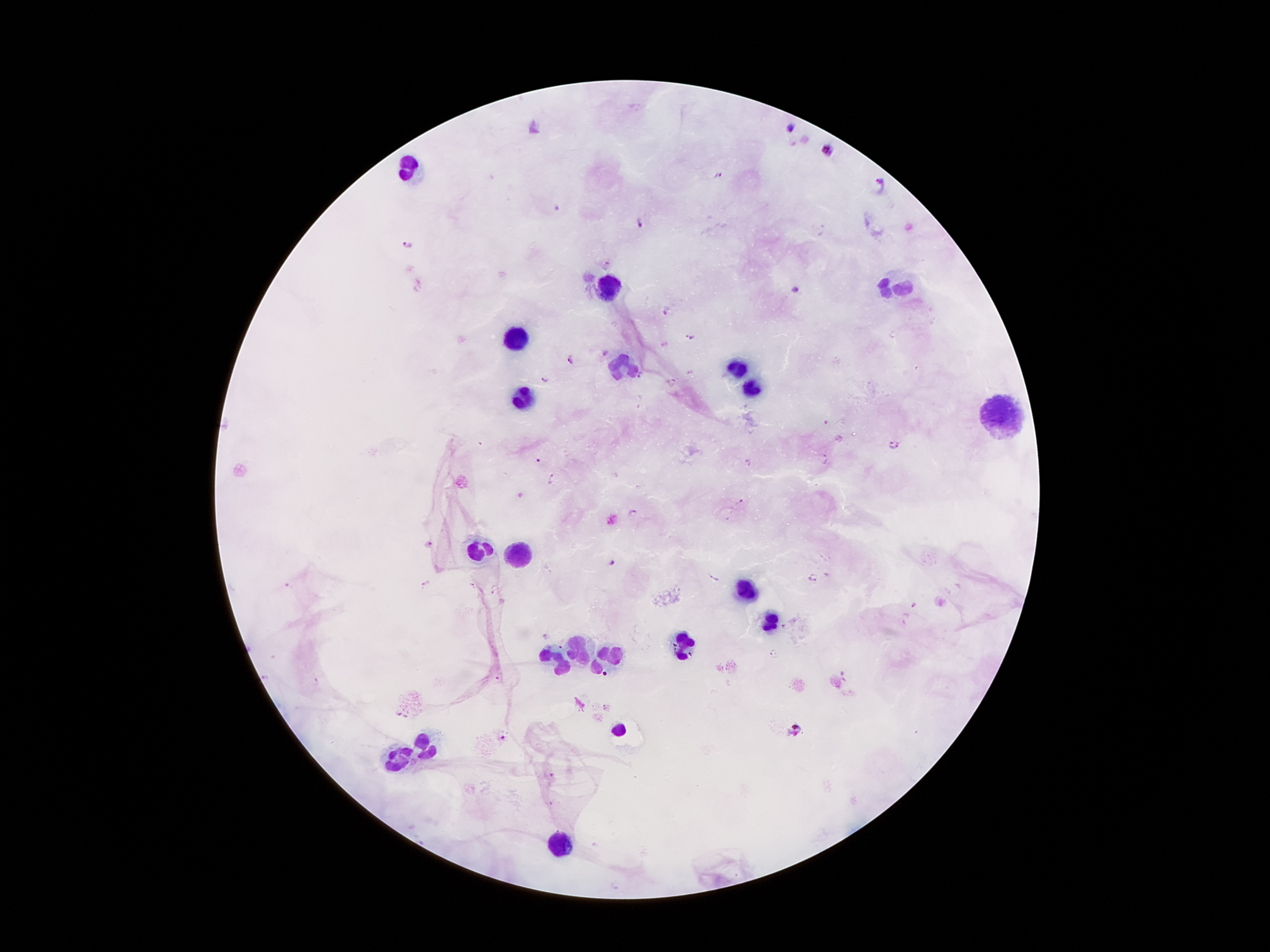

{
  "field_of_view": "one from this slide",
  "leukocyte_locations": "approximate centers as (x, y) in pixels: (408, 168), (609, 284), (897, 286), (517, 336), (622, 367), (739, 370), (752, 388), (523, 397), (1002, 412), (478, 552), (514, 554), (746, 588), (771, 620), (681, 641), (578, 648), (556, 659), (605, 659), (616, 731), (430, 745), (400, 755), (559, 843)",
  "stain": "Giemsa",
  "magnification": "100x",
  "image_size": "1270×952 pixels",
  "plasmodium_parasite_locations": "approximate centers as (x, y) in pixels: (789, 129), (828, 149), (717, 173), (880, 182), (555, 210), (639, 223), (407, 244), (796, 288), (667, 310), (689, 337), (605, 354), (570, 359), (641, 374), (547, 380), (673, 382), (827, 422), (893, 444), (824, 458), (538, 461), (749, 463), (551, 478), (739, 501), (631, 513), (429, 545), (613, 564), (814, 577), (713, 578), (427, 583), (289, 584), (473, 586), (495, 589), (915, 605), (545, 637), (774, 655), (605, 673), (500, 676), (266, 678), (399, 713), (796, 730), (502, 737), (552, 775)",
  "preparation": "thick blood smear",
  "patient_malaria_status": "infected with Plasmodium falciparum",
  "capture": "smartphone camera through the microscope eyepiece"
}